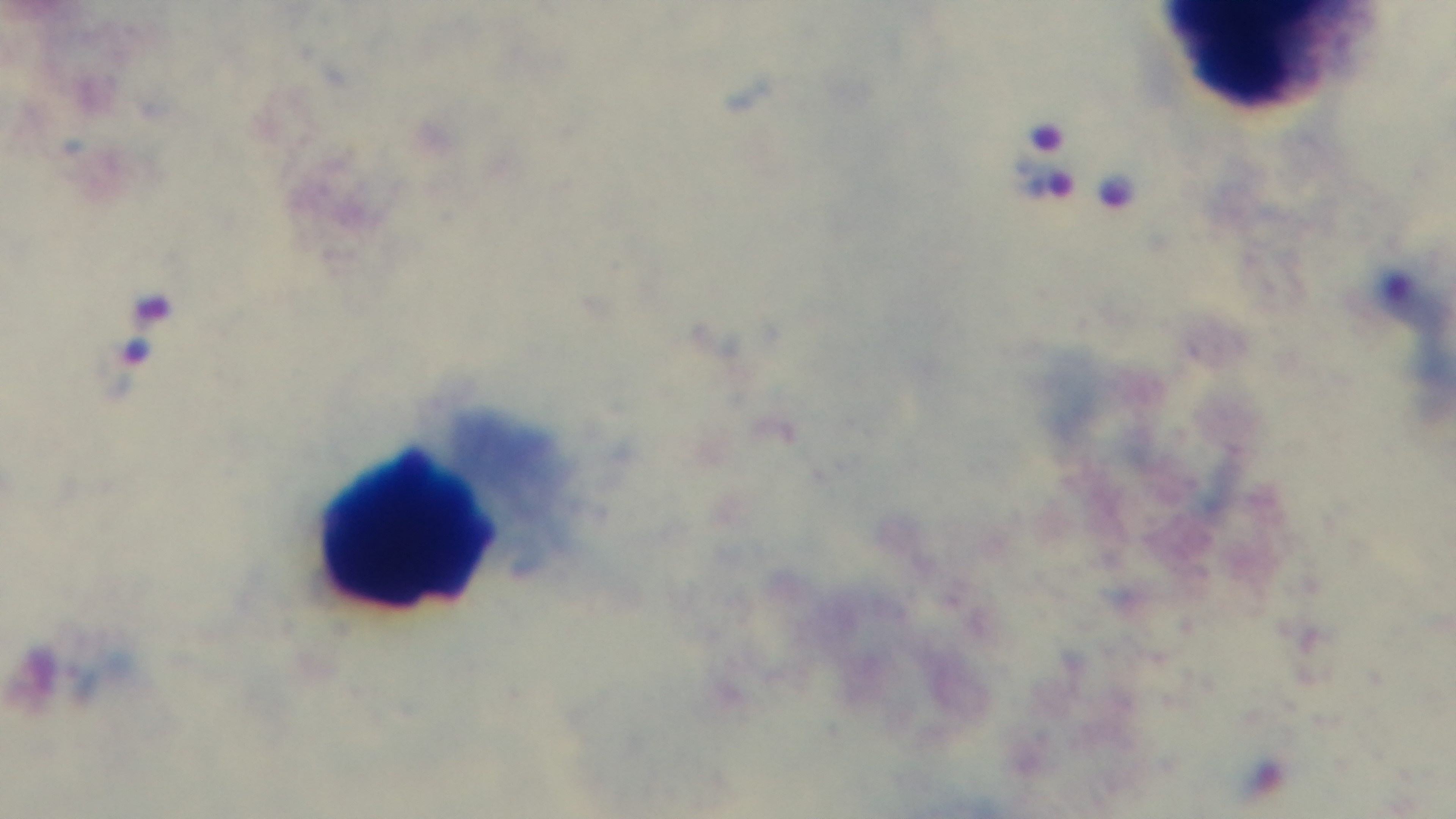
field of view = single
preparation = thick
malaria status = positive
stain = Giemsa
objective = 100x oil immersion
modality = light microscopy
capture = mounted 4K digital camera